Assess the morphology of the erythrocytes.
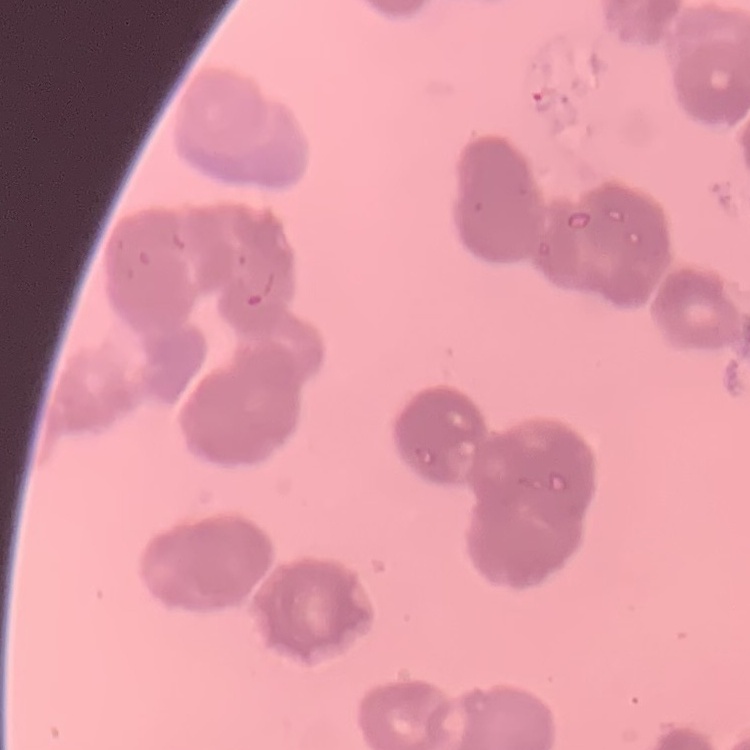
Rouleaux formation.

Thin blood smear. One tile cut from a larger photomicrograph. Stained with either Field's or Giemsa.